Identify the preparation type.
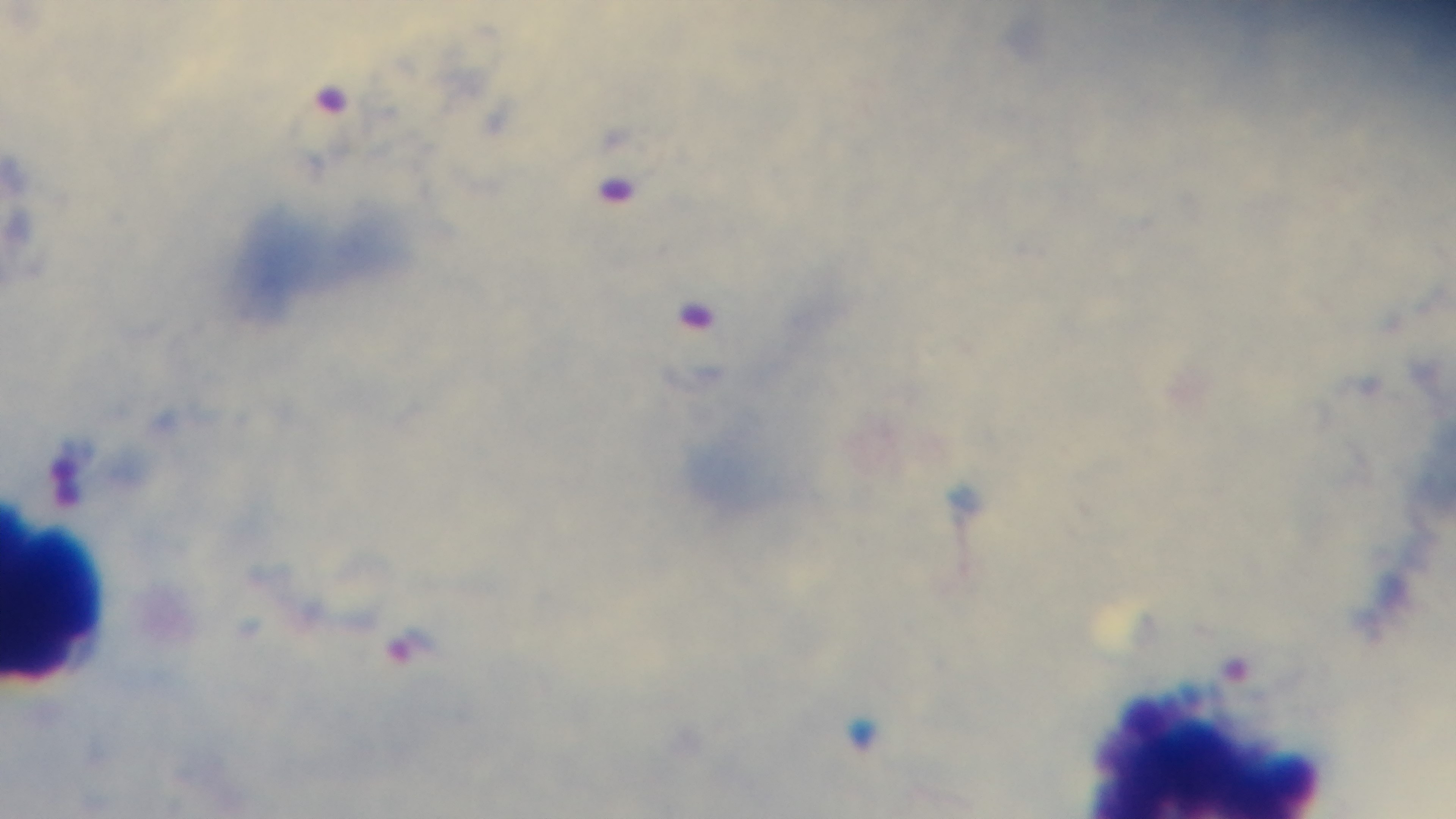

It is a thick blood film.

Summary:
  - Malaria status: infected
  - Stain: Giemsa
  - Field of view: single
  - Capture: mounted 4K digital camera
  - Objective: 100x oil immersion
  - Modality: light microscopy